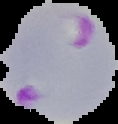
Summary:
  - Malaria status: parasitized
  - Preparation: thin blood film
  - Image size: 118×124 pixels
  - Image type: segmented cell region with the area outside set to black